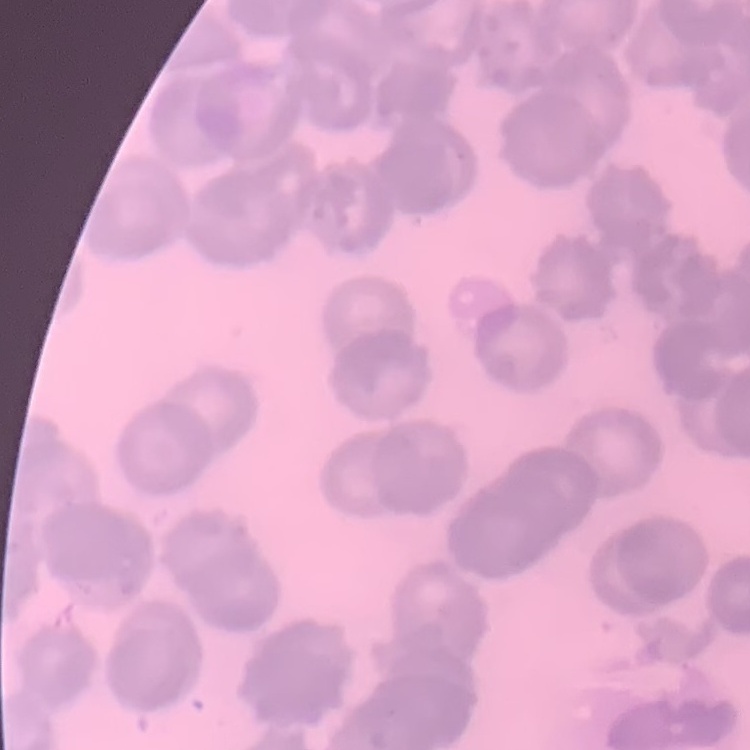
Summary:
  - Erythrocyte morphology: rouleaux formation
  - Preparation: thin blood film
  - Image type: one tile cut from a larger photomicrograph
  - Stain: Field's or Giemsa